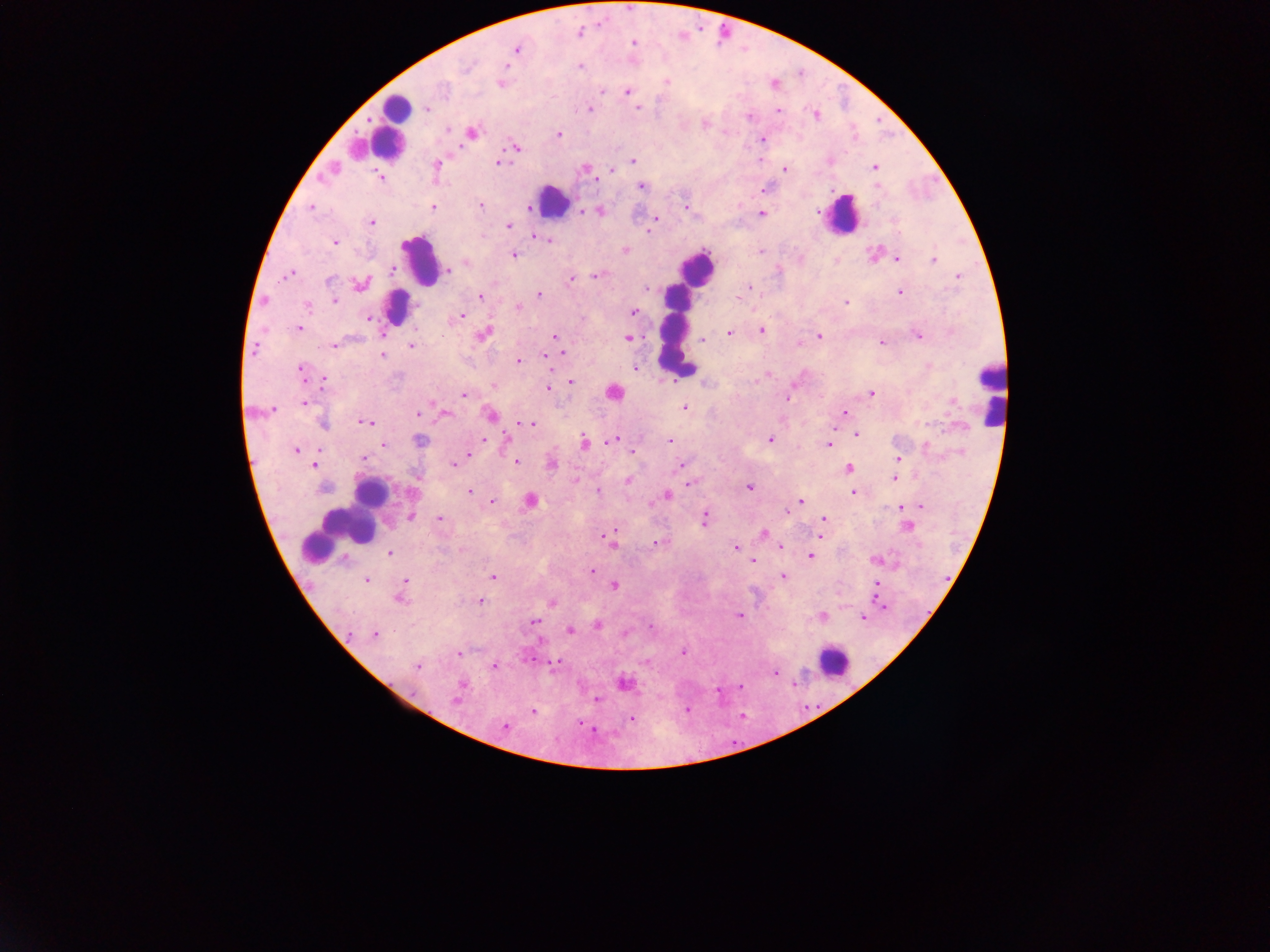
field of view = single
capture = mobile-phone photograph through a microscope
malaria parasite locations = approximate centers as (x, y) in pixels: (579, 32), (632, 42), (517, 49), (580, 66), (501, 82), (666, 83), (774, 83), (601, 89), (627, 92), (425, 107), (638, 107), (589, 108), (778, 110), (815, 114), (702, 123), (448, 129), (471, 132), (558, 134), (762, 139), (515, 148), (632, 160), (760, 160), (497, 162), (436, 164), (874, 167), (585, 169), (783, 169), (612, 171), (380, 177), (640, 186), (766, 187), (525, 205), (480, 206), (312, 207), (433, 207), (687, 207), (582, 210), (599, 210), (761, 213), (655, 218), (371, 221), (508, 225), (649, 232), (535, 235), (541, 238), (549, 240), (334, 242), (624, 249), (760, 251), (874, 253), (513, 254), (836, 259), (896, 259), (933, 259), (465, 261), (390, 269), (447, 269), (288, 274), (597, 275), (958, 276), (569, 280), (360, 284), (750, 287), (646, 289), (900, 292), (480, 295), (539, 295), (735, 298), (335, 299), (846, 302), (307, 306), (518, 307), (634, 312), (461, 316), (370, 318), (298, 327), (761, 330), (729, 333), (482, 334), (819, 335), (554, 336), (918, 336), (628, 338), (702, 339), (797, 343), (881, 343), (335, 344), (411, 346), (561, 353), (382, 355), (550, 355), (518, 361), (634, 368), (301, 369), (766, 374), (323, 380), (571, 382), (495, 385), (548, 388), (613, 391), (869, 392), (463, 394), (788, 398), (304, 402), (684, 406), (271, 409), (417, 412), (845, 412), (444, 413), (491, 415), (365, 421), (321, 424), (531, 424), (855, 433), (483, 439), (613, 439), (770, 439), (507, 440), (668, 440), (418, 441), (583, 441), (828, 444), (384, 445), (297, 450), (632, 453), (468, 455), (364, 458), (898, 459), (516, 462), (455, 463), (551, 463), (314, 464), (681, 464), (848, 468), (417, 478), (894, 478), (629, 480), (575, 482), (690, 483), (748, 487), (470, 491), (597, 491), (852, 491), (667, 495), (491, 501), (530, 501), (800, 501), (920, 505), (901, 506), (786, 513), (410, 517), (439, 519), (705, 519), (823, 519), (907, 526), (602, 534), (763, 534), (820, 535), (612, 542), (659, 542), (736, 548), (781, 548), (390, 553), (810, 556), (750, 558), (875, 559), (753, 561), (592, 571), (491, 576), (783, 577), (366, 580), (876, 583), (404, 584), (614, 585), (876, 595), (399, 596), (478, 601), (880, 602), (551, 603), (738, 615), (821, 616), (862, 617), (535, 621), (597, 624), (650, 627), (569, 630), (624, 633), (374, 634), (458, 653), (682, 653), (556, 662), (416, 666), (495, 666), (774, 672), (623, 683), (460, 686), (740, 686), (457, 697), (597, 699), (686, 710), (533, 712), (631, 719), (581, 725), (504, 726)
leukocyte locations = approximate centers as (x, y) in pixels: (395, 109), (391, 122), (357, 147), (551, 201), (841, 215), (419, 259), (697, 268), (395, 308), (674, 329), (990, 392), (368, 499), (345, 522), (831, 661)
image size = 1270×952 pixels
country = Ghana
preparation = thick blood smear